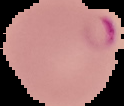
{
  "image_size": "124×106 pixels",
  "result": "Plasmodium parasites identified",
  "image_type": "segmented cell region with the area outside set to black",
  "preparation": "thin blood film"
}